Identify the parasite.
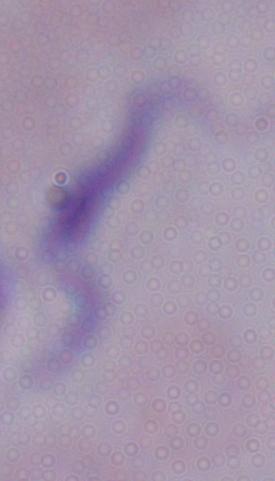

This is a trypanosome.

Captured at 1000x magnification. Micrograph.